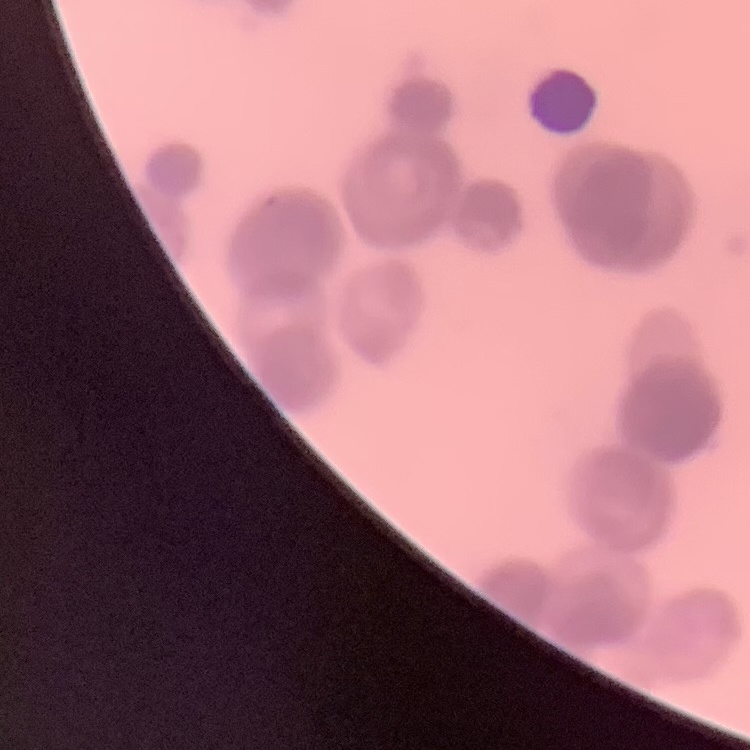
{
  "red_blood_cell_morphology": "rouleaux formation",
  "image_type": "square crop of a larger photomicrograph",
  "preparation": "thin blood film",
  "stain": "Field's or Giemsa"
}